Locate every Plasmodium ovale-infected red blood cell.
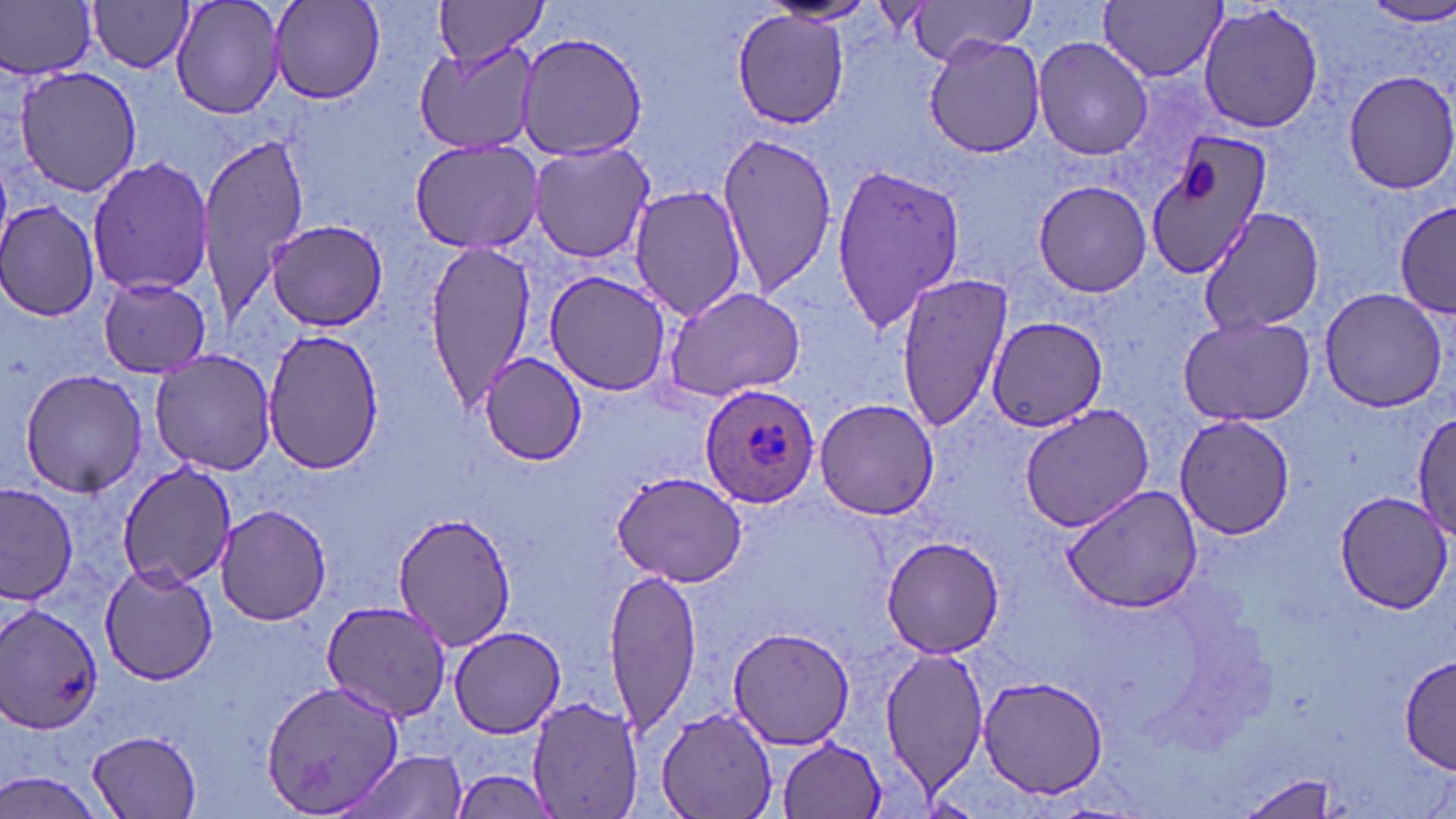

Approximate bounding boxes as (x1, y1, x2, y2) in pixels.
Plasmodium ovale-infected red blood cells: (698, 383, 822, 508).

slide-level diagnosis = Plasmodium ovale
modality = light microscopy
preparation = thin blood film
image size = 1456×819 pixels
field of view = single
platelet locations = approximate bounding boxes as (x1, y1, x2, y2) in pixels: (1183, 160, 1217, 201)
uninfected red blood cell locations = approximate bounding boxes as (x1, y1, x2, y2) in pixels: (1, 0, 98, 81), (171, 0, 286, 120), (268, 0, 384, 104), (900, 0, 1040, 61), (87, 1, 196, 73), (431, 1, 550, 62), (761, 1, 881, 26), (1099, 1, 1226, 83), (1360, 1, 1456, 26), (1197, 2, 1325, 137), (731, 10, 848, 130), (516, 29, 649, 162), (924, 33, 1048, 158), (1033, 34, 1153, 161), (413, 39, 543, 154), (13, 64, 144, 198), (1339, 69, 1456, 197), (196, 132, 310, 317), (1146, 133, 1274, 279), (712, 134, 838, 298), (410, 136, 548, 254), (527, 140, 658, 264), (87, 157, 215, 297), (830, 162, 964, 334), (1032, 179, 1153, 299), (628, 185, 747, 321), (1396, 199, 1456, 313), (0, 201, 102, 322), (1193, 206, 1328, 337), (265, 220, 392, 331), (422, 241, 541, 411), (543, 269, 670, 396), (896, 271, 1014, 431), (97, 277, 213, 377), (658, 285, 809, 405), (1318, 286, 1449, 413), (1176, 313, 1317, 427), (986, 317, 1107, 431), (259, 329, 388, 477), (149, 351, 275, 475), (479, 353, 583, 464), (18, 369, 149, 497), (813, 398, 941, 520), (1017, 404, 1159, 532), (1411, 409, 1456, 543), (1173, 415, 1295, 539), (117, 462, 236, 589), (609, 469, 749, 587), (1062, 482, 1206, 614), (1, 483, 78, 605), (1333, 487, 1453, 613), (216, 507, 332, 627), (394, 511, 517, 649), (880, 535, 1006, 659), (99, 565, 220, 685), (602, 568, 703, 737), (318, 600, 454, 722), (2, 604, 103, 736), (727, 625, 855, 749), (449, 626, 566, 738), (878, 645, 989, 793), (1398, 655, 1452, 772), (977, 676, 1109, 799), (261, 680, 406, 816), (526, 696, 643, 816), (654, 709, 779, 819), (90, 730, 205, 817), (776, 737, 888, 819), (348, 751, 468, 819), (449, 767, 559, 819), (0, 771, 111, 819), (1234, 773, 1342, 817)
magnification = 1000x
stain = May-Grünwald-Giemsa